Locate and identify every blood parasite.
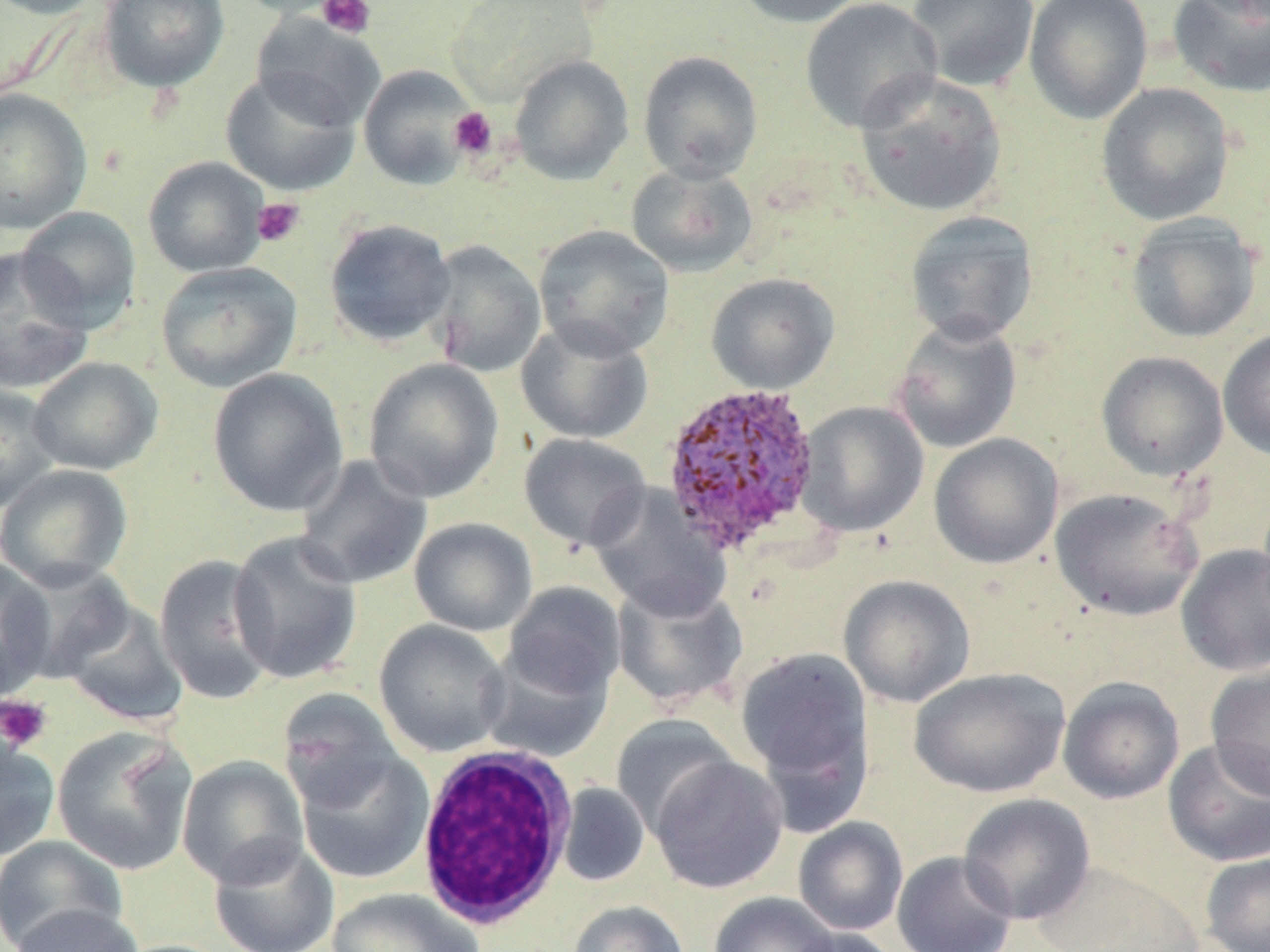
Approximate bounding boxes as (x1, y1, x2, y2) in pixels.
Plasmodium ovale-infected red blood cells: (659, 382, 822, 554).
No Plasmodium falciparum, Plasmodium malariae, Plasmodium vivax, Babesia divergens, or Trypanosoma brucei observed.

Summary:
  - Uninfected red blood cell locations: (0, 0, 105, 19), (97, 0, 230, 92), (231, 0, 352, 18), (732, 0, 868, 28), (799, 0, 942, 134), (906, 0, 1039, 92), (1024, 0, 1153, 124), (1167, 0, 1270, 99), (250, 14, 385, 131), (638, 50, 763, 183), (509, 55, 633, 185), (358, 64, 479, 190), (220, 69, 360, 196), (854, 71, 1007, 218), (1095, 82, 1234, 226), (0, 87, 92, 234), (143, 156, 270, 277), (625, 163, 759, 278), (17, 206, 142, 332), (904, 210, 1039, 346), (1125, 213, 1262, 343), (324, 218, 457, 348), (532, 225, 675, 360), (423, 239, 547, 378), (0, 247, 94, 394), (155, 261, 302, 393), (705, 273, 840, 394), (515, 317, 654, 444), (890, 317, 1022, 454), (1218, 329, 1270, 461), (1096, 350, 1229, 481), (26, 357, 164, 476), (363, 357, 504, 504), (207, 367, 349, 517), (0, 382, 63, 512), (795, 401, 929, 537), (518, 433, 652, 553), (929, 433, 1064, 569), (293, 453, 433, 590), (1, 464, 134, 591), (587, 484, 732, 620), (1050, 487, 1202, 621), (409, 517, 538, 636), (227, 530, 364, 685), (1176, 544, 1270, 676), (153, 554, 278, 705), (0, 559, 57, 696), (6, 562, 136, 684), (837, 574, 976, 707), (611, 578, 748, 710), (502, 582, 626, 700), (59, 598, 189, 728), (373, 619, 511, 757), (478, 644, 615, 764), (735, 647, 873, 791), (1205, 664, 1270, 800), (910, 667, 1069, 798), (1057, 676, 1185, 805), (278, 688, 405, 811), (611, 714, 739, 835), (51, 725, 197, 876), (0, 732, 60, 862), (1163, 738, 1270, 868), (295, 749, 435, 884), (177, 755, 309, 888), (649, 755, 788, 894), (555, 782, 650, 887), (958, 792, 1096, 925), (793, 817, 909, 936), (0, 835, 128, 951), (208, 837, 339, 952), (892, 850, 1018, 952), (1200, 851, 1270, 952), (1033, 861, 1202, 952), (325, 888, 484, 952), (708, 892, 839, 952), (568, 900, 690, 952), (8, 903, 146, 952), (788, 926, 898, 952)
  - White blood cell locations: (414, 745, 579, 930)
  - Platelet locations: (317, 0, 376, 40), (450, 107, 498, 161), (251, 198, 305, 248), (0, 695, 52, 753)
  - Slide-level diagnosis: Plasmodium ovale
  - Preparation: thin blood smear
  - Magnification: 1000x
  - Field of view: single
  - Image size: 1270×952 pixels
  - Stain: May-Grünwald-Giemsa
  - Modality: light microscopy